State the blood parasite species.
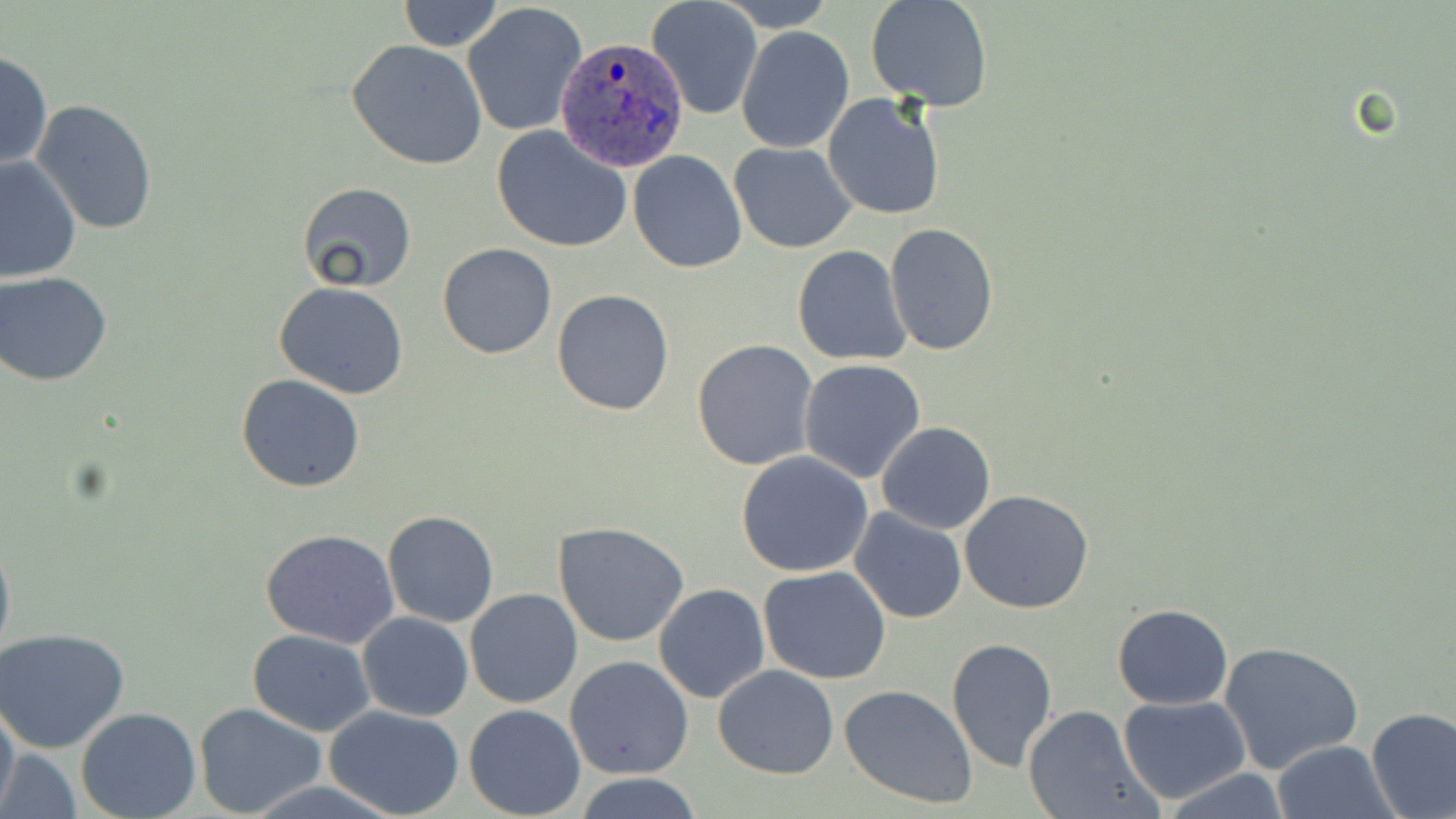

Plasmodium ovale.

Approximate bounding boxes as named x1/y1/x2/y2 corners in pixels. Uninfected red blood cell locations: (x1=397, y1=0, x2=503, y2=51), (x1=647, y1=0, x2=763, y2=121), (x1=720, y1=0, x2=836, y2=31), (x1=865, y1=1, x2=993, y2=111), (x1=462, y1=3, x2=588, y2=139), (x1=737, y1=27, x2=855, y2=153), (x1=347, y1=39, x2=489, y2=171), (x1=0, y1=50, x2=50, y2=171), (x1=823, y1=92, x2=947, y2=222), (x1=32, y1=99, x2=158, y2=235), (x1=491, y1=126, x2=631, y2=252), (x1=729, y1=141, x2=858, y2=253), (x1=627, y1=150, x2=747, y2=274), (x1=0, y1=155, x2=81, y2=283), (x1=296, y1=181, x2=418, y2=292), (x1=884, y1=222, x2=999, y2=359), (x1=437, y1=242, x2=557, y2=359), (x1=793, y1=245, x2=911, y2=366), (x1=1, y1=272, x2=116, y2=387), (x1=274, y1=282, x2=408, y2=399), (x1=552, y1=289, x2=675, y2=415), (x1=692, y1=339, x2=819, y2=471), (x1=799, y1=358, x2=926, y2=482), (x1=237, y1=375, x2=366, y2=492), (x1=877, y1=421, x2=996, y2=534), (x1=735, y1=450, x2=876, y2=577), (x1=960, y1=489, x2=1095, y2=613), (x1=848, y1=508, x2=967, y2=624), (x1=383, y1=510, x2=498, y2=627), (x1=553, y1=522, x2=692, y2=648), (x1=0, y1=528, x2=15, y2=670), (x1=259, y1=529, x2=401, y2=648), (x1=758, y1=565, x2=891, y2=684), (x1=653, y1=582, x2=770, y2=704), (x1=463, y1=589, x2=584, y2=709), (x1=1112, y1=603, x2=1233, y2=709), (x1=358, y1=612, x2=473, y2=721), (x1=0, y1=627, x2=131, y2=753), (x1=247, y1=629, x2=375, y2=736), (x1=946, y1=637, x2=1058, y2=770), (x1=1218, y1=641, x2=1363, y2=773), (x1=565, y1=655, x2=694, y2=779), (x1=713, y1=666, x2=839, y2=779), (x1=840, y1=684, x2=981, y2=809), (x1=1118, y1=695, x2=1250, y2=803), (x1=0, y1=697, x2=20, y2=817), (x1=194, y1=704, x2=327, y2=819), (x1=463, y1=704, x2=586, y2=818), (x1=1022, y1=704, x2=1158, y2=819), (x1=324, y1=705, x2=466, y2=818), (x1=1365, y1=706, x2=1456, y2=819), (x1=75, y1=708, x2=201, y2=819), (x1=1271, y1=740, x2=1396, y2=819), (x1=2, y1=746, x2=79, y2=819), (x1=1159, y1=768, x2=1290, y2=818), (x1=574, y1=773, x2=706, y2=818). Plasmodium ovale-infected red blood cell locations: (x1=553, y1=37, x2=691, y2=174). One field of a larger specimen. Captured at 1000x magnification. Thin blood film. Image is 1456×819 pixels. Light microscopy. May-Grünwald-Giemsa stain.